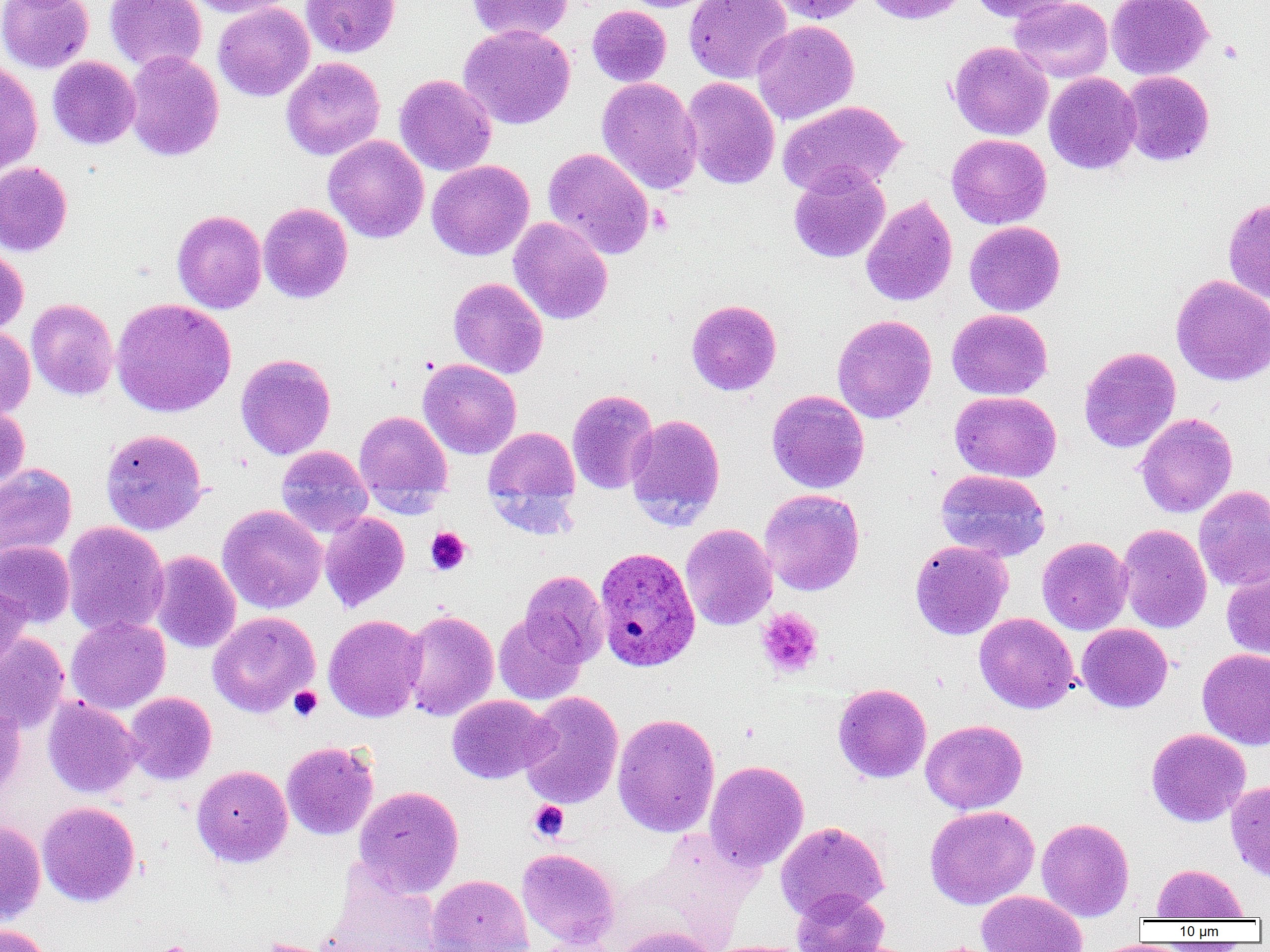
Summary:
  - Coordinate format: approximate bounding boxes as (x1,y1)-(x2,y2) corner pairs in pixels
  - Platelet locations: (425,527)-(471,575), (756,608)-(824,678), (289,686)-(322,721), (529,801)-(569,842), (149,941)-(201,952)
  - Uninfected red blood cell locations: (0,0)-(94,73), (105,0)-(207,73), (184,0)-(296,18), (301,0)-(400,58), (466,0)-(574,42), (619,0)-(719,12), (684,0)-(792,84), (768,0)-(868,23), (865,0)-(968,25), (967,0)-(1078,22), (1008,0)-(1113,83), (1106,0)-(1213,80), (213,2)-(314,102), (587,5)-(672,87), (751,20)-(859,125), (458,24)-(575,129), (948,41)-(1053,140), (124,51)-(224,161), (47,56)-(140,149), (281,56)-(385,160), (0,61)-(43,175), (1120,71)-(1214,166), (1044,72)-(1141,174), (395,74)-(497,176), (597,77)-(703,195), (681,77)-(780,189), (778,100)-(907,196), (946,134)-(1051,229), (323,135)-(429,243), (543,147)-(654,259), (426,160)-(534,260), (0,162)-(72,257), (789,164)-(890,263), (861,195)-(958,306), (1223,197)-(1270,302), (258,203)-(353,303), (172,210)-(267,313), (508,217)-(613,324), (965,221)-(1065,315), (0,245)-(28,335), (1171,274)-(1270,386), (448,277)-(548,379), (26,298)-(118,400), (111,298)-(236,417), (686,299)-(781,395), (947,309)-(1052,399), (832,314)-(936,423), (0,325)-(35,420), (1079,346)-(1181,453), (236,354)-(336,459), (418,358)-(521,459), (567,389)-(659,494), (767,390)-(869,493), (950,390)-(1061,482), (0,405)-(30,491), (354,409)-(453,509), (625,413)-(726,530), (1135,413)-(1237,518), (484,427)-(580,515), (100,428)-(207,535), (276,445)-(372,538), (0,463)-(77,559), (936,469)-(1051,562), (1194,486)-(1270,591), (759,489)-(865,596), (217,505)-(327,614), (320,512)-(410,612), (61,521)-(169,637), (680,524)-(777,630), (1116,524)-(1213,633), (1037,537)-(1133,635), (909,539)-(1013,640), (0,541)-(75,627), (149,551)-(241,653), (1222,570)-(1270,660), (520,571)-(608,667), (0,576)-(30,673), (401,609)-(499,721), (207,611)-(320,717), (494,611)-(587,705), (975,612)-(1079,714), (323,614)-(427,722), (66,616)-(170,714), (1076,623)-(1173,713), (0,633)-(69,734), (1197,648)-(1270,750), (833,683)-(932,783), (124,691)-(216,785), (518,691)-(624,809), (447,694)-(555,784), (43,697)-(140,798), (0,701)-(25,801), (612,713)-(720,837), (920,719)-(1027,814), (1146,728)-(1250,826), (281,741)-(379,840), (705,760)-(808,871), (192,765)-(292,866), (1226,779)-(1270,881), (353,785)-(464,896), (37,801)-(140,907), (925,805)-(1039,909), (1036,818)-(1135,920), (0,819)-(46,924), (776,821)-(889,921), (517,848)-(620,948), (327,863)-(442,952), (1152,863)-(1247,920), (426,875)-(533,952), (791,889)-(889,952), (976,890)-(1088,952), (0,923)-(53,952), (614,926)-(718,952), (530,934)-(625,952), (708,940)-(815,952)
  - Plasmodium ovale-infected red blood cell locations: (594,546)-(700,671)
  - Slide-level diagnosis: Plasmodium ovale
  - Field of view: one of a larger specimen
  - Magnification: 1000x
  - Image size: 1270×952 pixels
  - Modality: light microscopy
  - Preparation: thin blood smear